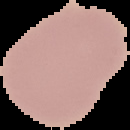 From a thin blood film. Segmented cell region on a black background. Image is 130×130 pixels. Result: no malaria parasites seen.